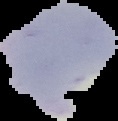
From a thin blood film. The area outside the segmented cell region is set to black. Image is 118×121 pixels. Malaria status: parasitized.